Classify this cell by malaria status.
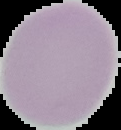
Uninfected.

Summary:
  - Preparation: thin blood film
  - Image type: segmented cell region with the area outside set to black
  - Image size: 121×130 pixels